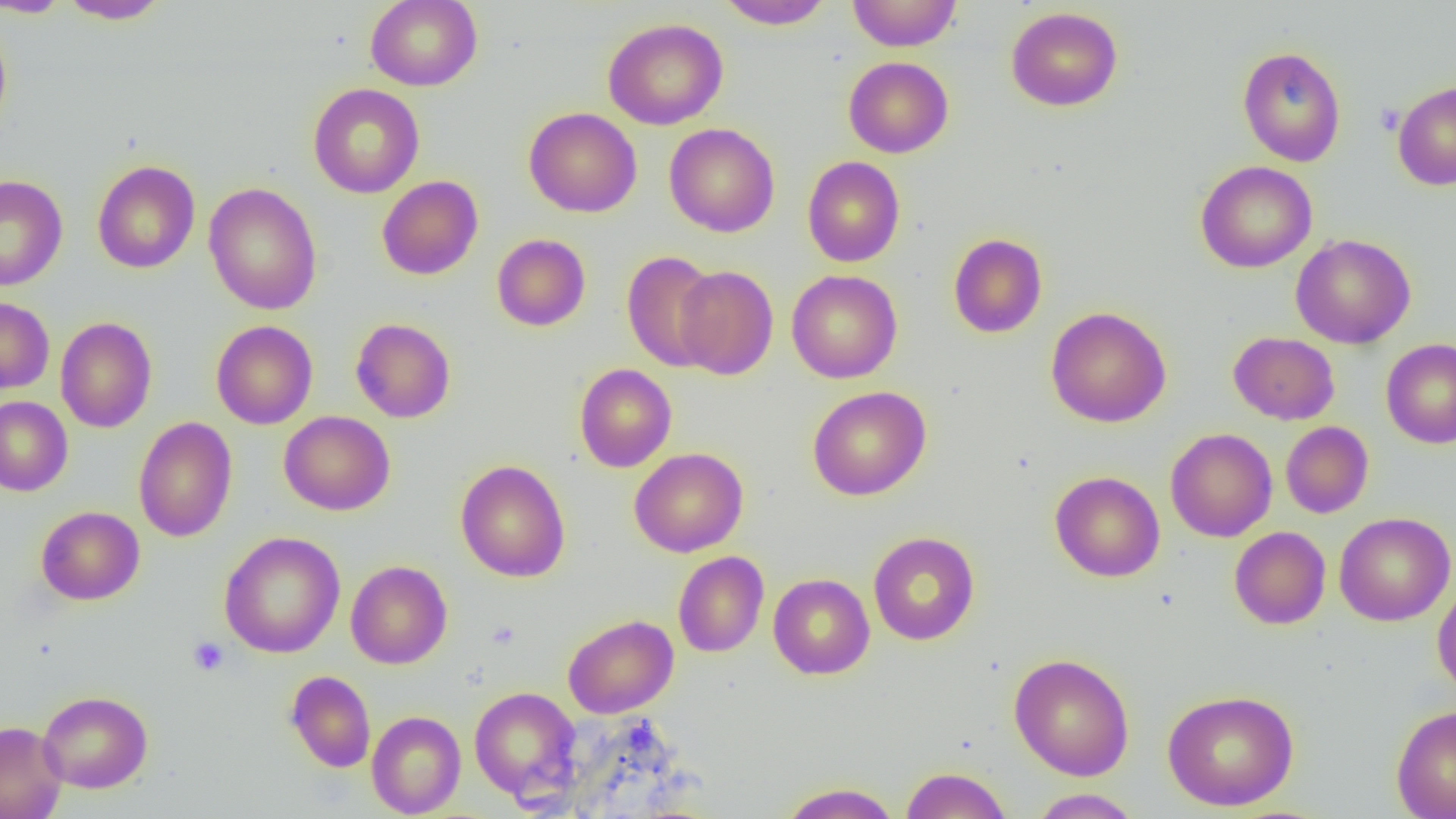
Summary:
  - Coordinate format: approximate bounding boxes as (x1,y1)-(x2,y2) corner pairs in pixels
  - Platelet locations: (1376,104)-(1404,134), (188,636)-(229,676)
  - Uninfected red blood cell locations: (58,0)-(173,24), (365,0)-(483,91), (716,0)-(834,30), (847,0)-(961,51), (0,1)-(73,18), (1006,6)-(1123,111), (0,18)-(13,141), (603,18)-(729,130), (1237,46)-(1346,167), (843,56)-(954,158), (1392,81)-(1456,191), (307,83)-(424,198), (523,107)-(642,217), (664,123)-(780,237), (802,156)-(905,267), (91,159)-(200,274), (1195,160)-(1317,273), (0,175)-(68,291), (377,176)-(483,280), (204,182)-(322,315), (948,233)-(1047,338), (1290,233)-(1416,349), (492,234)-(591,331), (622,250)-(721,372), (674,266)-(778,380), (786,269)-(903,383), (800,269)-(910,502), (0,296)-(54,393), (1046,306)-(1172,427), (56,317)-(157,433), (351,318)-(456,423), (211,320)-(318,429), (1228,332)-(1340,425), (1380,338)-(1456,449), (574,364)-(677,472), (807,385)-(931,500), (0,396)-(73,496), (279,411)-(395,515), (134,416)-(238,542), (1280,421)-(1374,518), (1165,428)-(1277,542), (629,448)-(748,557), (456,459)-(570,582), (1050,470)-(1165,582), (35,506)-(145,605), (1334,511)-(1455,626), (1229,526)-(1331,629), (219,531)-(345,658), (868,531)-(980,645), (673,551)-(768,657), (346,560)-(453,669), (768,573)-(875,679), (1432,579)-(1456,698), (563,614)-(679,718), (1009,653)-(1134,781), (284,670)-(376,772), (469,686)-(581,805), (1161,689)-(1300,811), (38,690)-(153,793), (1390,704)-(1456,819), (366,711)-(466,817), (0,720)-(67,819), (900,766)-(1013,819), (778,782)-(901,819), (1028,788)-(1143,818)
  - Slide-level diagnosis: no evidence of blood parasites
  - Image size: 1456×819 pixels
  - Magnification: 1000x
  - Field of view: single
  - Preparation: thin blood smear
  - Modality: light microscopy